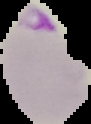
Summary:
  - Image type: cell region segmented out of the field of view; surrounding area masked to black
  - Image size: 91×124 pixels
  - Preparation: thin blood film
  - Malaria status: parasitized